Mark where platelets are.
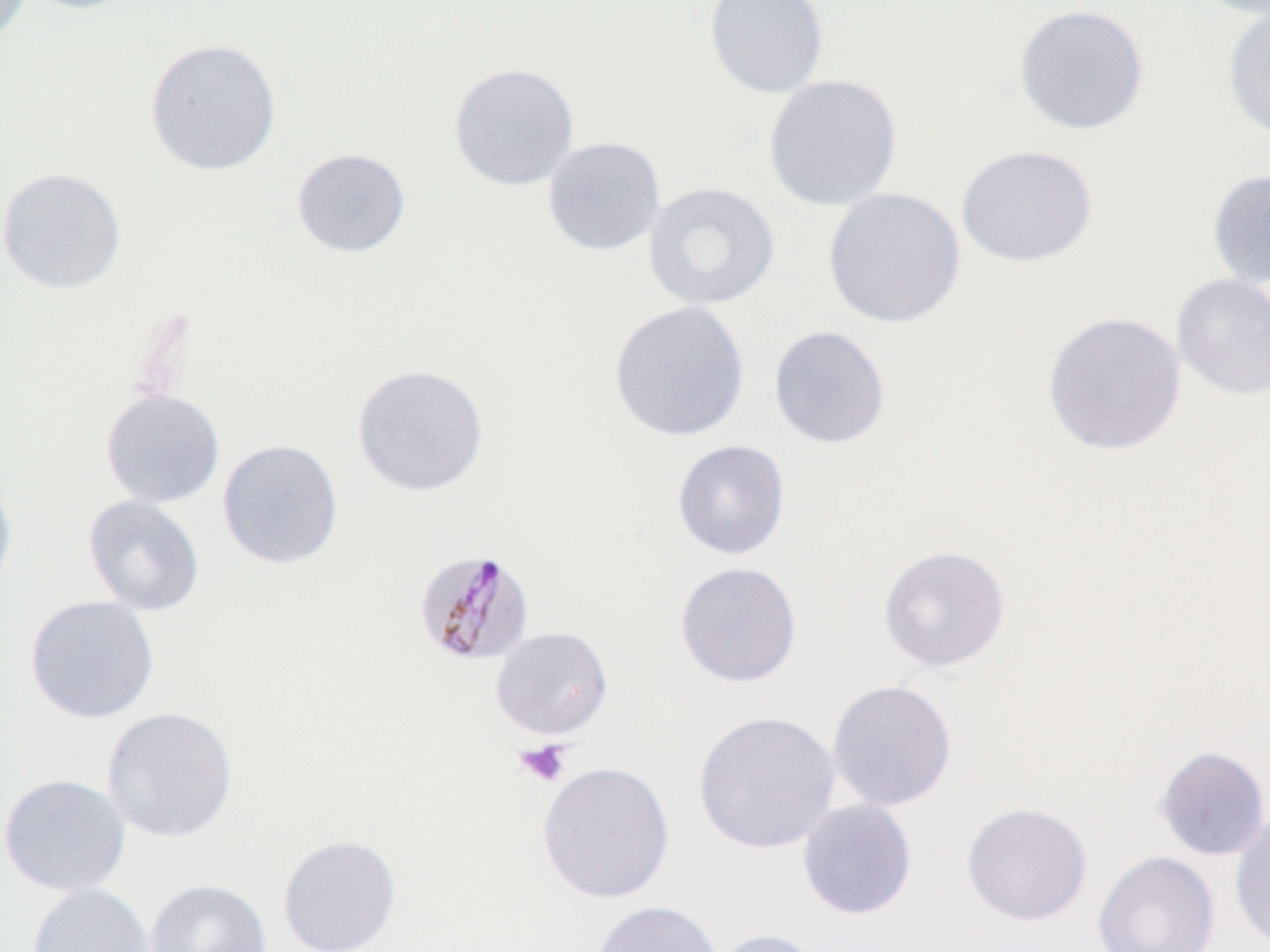

Approximate bounding boxes as [x1, y1, x2, y2] in pixels.
Platelets: [514, 739, 572, 787].

{
  "slide_level_diagnosis": "Plasmodium malariae",
  "magnification": "1000x",
  "stain": "May-Grünwald-Giemsa",
  "preparation": "thin blood smear",
  "modality": "light microscopy",
  "image_size": "1270×952 pixels",
  "field_of_view": "one of a larger specimen",
  "plasmodium_malariae_infected_red_blood_cell_locations": "approximate bounding boxes as [x1, y1, x2, y2] in pixels: [412, 546, 536, 668]",
  "uninfected_red_blood_cell_locations": "approximate bounding boxes as [x1, y1, x2, y2] in pixels: [0, 0, 32, 44], [21, 0, 145, 15], [703, 0, 829, 99], [1191, 0, 1270, 18], [1222, 2, 1270, 142], [1013, 4, 1150, 135], [144, 38, 282, 175], [448, 63, 579, 191], [763, 73, 902, 211], [542, 136, 666, 256], [956, 144, 1097, 267], [291, 148, 411, 258], [0, 167, 126, 295], [1207, 168, 1270, 289], [643, 181, 780, 311], [823, 187, 966, 328], [1171, 273, 1270, 400], [608, 299, 750, 442], [1042, 311, 1187, 455], [769, 324, 891, 449], [351, 363, 489, 497], [100, 389, 225, 508], [217, 438, 344, 570], [672, 439, 791, 560], [0, 472, 17, 596], [82, 494, 205, 616], [877, 544, 1011, 673], [674, 561, 802, 687], [25, 595, 160, 723], [490, 626, 613, 739], [826, 679, 957, 812], [101, 706, 238, 843], [692, 710, 841, 854], [1154, 746, 1270, 860], [536, 761, 675, 904], [0, 773, 132, 897], [797, 798, 918, 920], [961, 802, 1093, 926], [1230, 812, 1270, 951], [278, 834, 401, 952], [1092, 850, 1220, 952], [144, 879, 271, 952], [27, 882, 156, 952], [589, 900, 723, 952], [711, 928, 829, 952]"
}